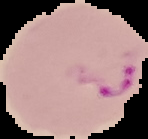
Image is 148×139 pixels. Malaria status: parasitized. From a thin blood film. The area outside the segmented cell region is set to black.